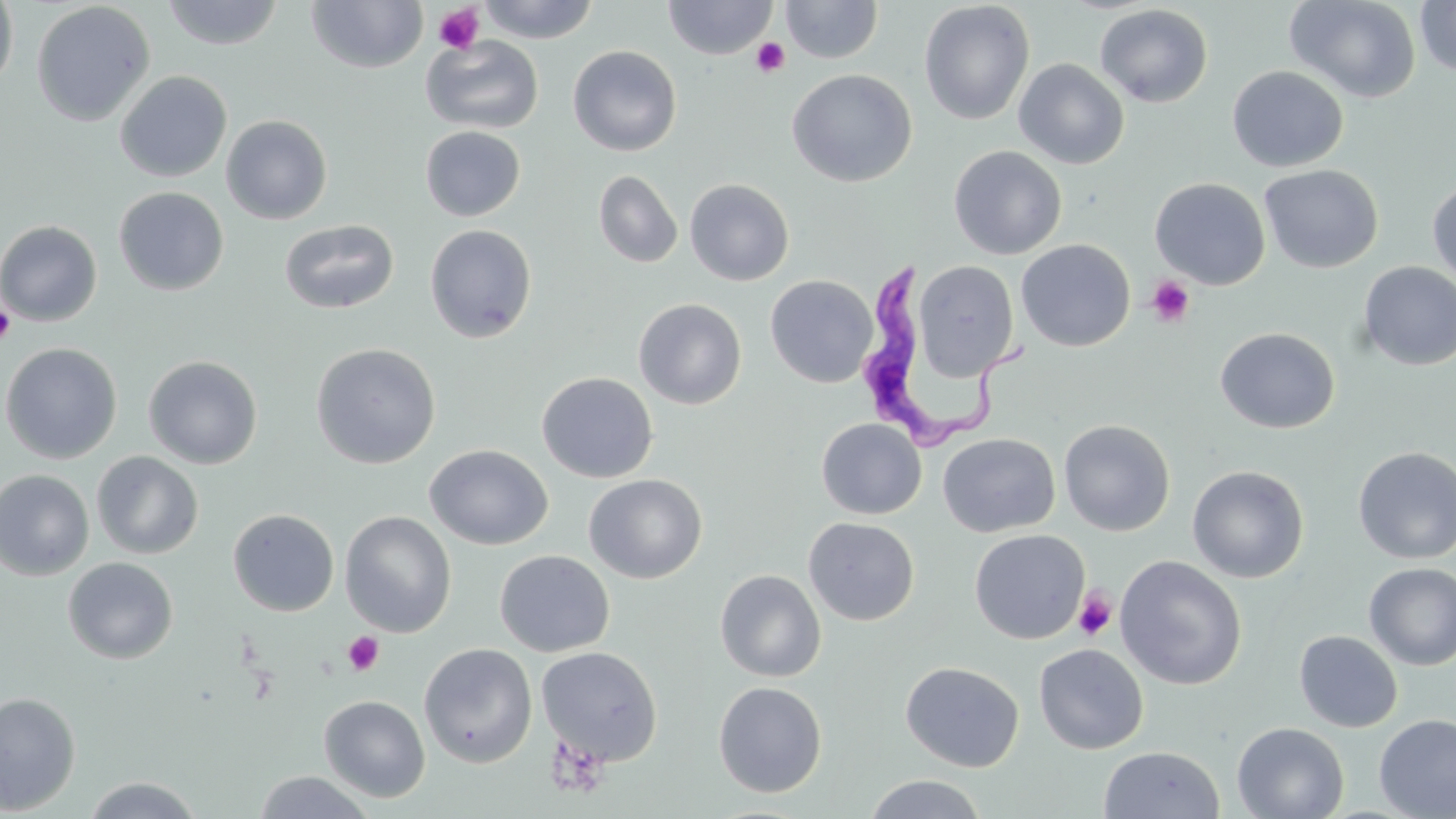

slide-level diagnosis = Trypanosoma brucei
magnification = 1000x
platelet locations = approximate bounding boxes as named x1/y1/x2/y2 corners in pixels: (x1=433, y1=3, x2=485, y2=55), (x1=750, y1=37, x2=790, y2=78), (x1=1146, y1=275, x2=1195, y2=328), (x1=0, y1=302, x2=16, y2=347), (x1=1074, y1=587, x2=1117, y2=642), (x1=343, y1=632, x2=384, y2=676), (x1=545, y1=735, x2=609, y2=798)
field of view = one of a larger specimen
uninfected red blood cell locations = approximate bounding boxes as named x1/y1/x2/y2 corners in pixels: (x1=161, y1=0, x2=286, y2=50), (x1=476, y1=0, x2=601, y2=43), (x1=663, y1=0, x2=778, y2=60), (x1=780, y1=0, x2=883, y2=63), (x1=1285, y1=0, x2=1422, y2=103), (x1=0, y1=1, x2=18, y2=94), (x1=31, y1=1, x2=155, y2=127), (x1=305, y1=1, x2=429, y2=74), (x1=1414, y1=1, x2=1456, y2=78), (x1=918, y1=2, x2=1035, y2=125), (x1=1094, y1=4, x2=1213, y2=108), (x1=420, y1=34, x2=544, y2=134), (x1=567, y1=45, x2=682, y2=156), (x1=1014, y1=59, x2=1130, y2=169), (x1=1227, y1=66, x2=1349, y2=172), (x1=787, y1=69, x2=918, y2=188), (x1=115, y1=70, x2=232, y2=182), (x1=220, y1=114, x2=333, y2=225), (x1=419, y1=125, x2=526, y2=222), (x1=949, y1=145, x2=1067, y2=260), (x1=1259, y1=164, x2=1384, y2=273), (x1=593, y1=170, x2=684, y2=269), (x1=1149, y1=177, x2=1271, y2=290), (x1=684, y1=178, x2=795, y2=286), (x1=1427, y1=180, x2=1456, y2=288), (x1=113, y1=186, x2=229, y2=295), (x1=279, y1=219, x2=400, y2=314), (x1=0, y1=220, x2=103, y2=327), (x1=423, y1=224, x2=538, y2=343), (x1=1016, y1=238, x2=1136, y2=352), (x1=912, y1=260, x2=1020, y2=380), (x1=1357, y1=262, x2=1456, y2=371), (x1=765, y1=275, x2=878, y2=388), (x1=633, y1=298, x2=746, y2=409), (x1=1215, y1=327, x2=1340, y2=434), (x1=0, y1=342, x2=122, y2=464), (x1=310, y1=342, x2=441, y2=469), (x1=143, y1=354, x2=263, y2=469), (x1=536, y1=371, x2=658, y2=483), (x1=816, y1=417, x2=927, y2=519), (x1=1058, y1=419, x2=1175, y2=536), (x1=938, y1=432, x2=1060, y2=537), (x1=425, y1=444, x2=554, y2=550), (x1=1353, y1=446, x2=1456, y2=565), (x1=91, y1=451, x2=204, y2=560), (x1=1187, y1=464, x2=1309, y2=583), (x1=0, y1=468, x2=95, y2=581), (x1=583, y1=473, x2=708, y2=583), (x1=228, y1=508, x2=340, y2=617), (x1=339, y1=510, x2=457, y2=637), (x1=803, y1=517, x2=920, y2=626), (x1=969, y1=529, x2=1090, y2=644), (x1=494, y1=550, x2=615, y2=657), (x1=1114, y1=555, x2=1248, y2=690), (x1=63, y1=557, x2=178, y2=664), (x1=1364, y1=562, x2=1456, y2=670), (x1=714, y1=569, x2=826, y2=682), (x1=1294, y1=630, x2=1402, y2=732), (x1=419, y1=643, x2=538, y2=768), (x1=1034, y1=643, x2=1149, y2=754), (x1=536, y1=645, x2=663, y2=766), (x1=900, y1=661, x2=1024, y2=772), (x1=713, y1=681, x2=827, y2=797), (x1=0, y1=691, x2=81, y2=815), (x1=318, y1=695, x2=431, y2=802), (x1=1373, y1=713, x2=1456, y2=819), (x1=1231, y1=722, x2=1349, y2=819), (x1=1098, y1=745, x2=1225, y2=819), (x1=252, y1=771, x2=377, y2=818), (x1=862, y1=773, x2=989, y2=819), (x1=80, y1=776, x2=206, y2=818)
Trypanosoma brucei locations = approximate bounding boxes as named x1/y1/x2/y2 corners in pixels: (x1=858, y1=257, x2=1032, y2=455)
stain = May-Grünwald-Giemsa
modality = optical microscopy
image size = 1456×819 pixels
preparation = thin blood smear